Describe the morphology of the red blood cells.
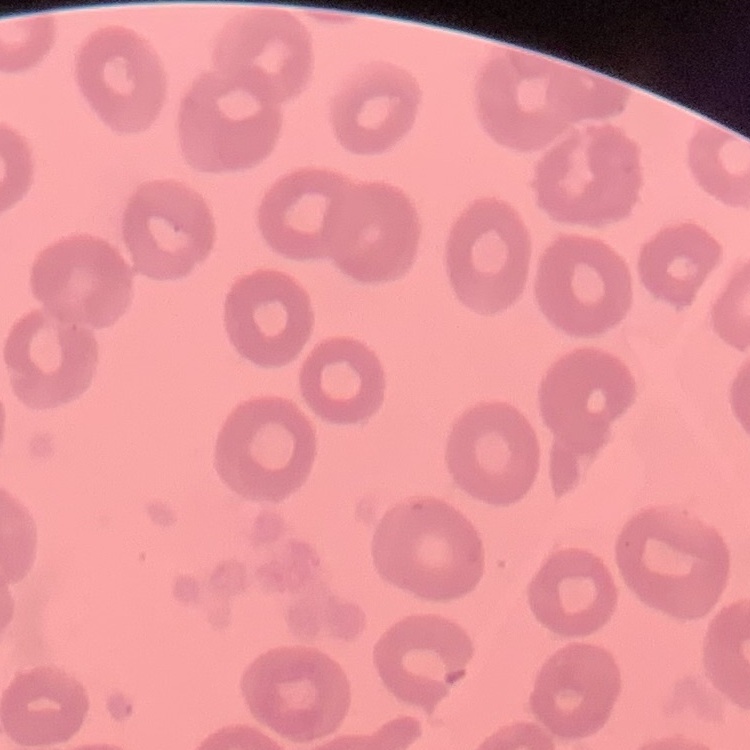

They show no rouleaux formation.

Summary:
  - Stain: Field's or Giemsa
  - Preparation: thin peripheral smear
  - Image type: one tile cut from a larger photomicrograph